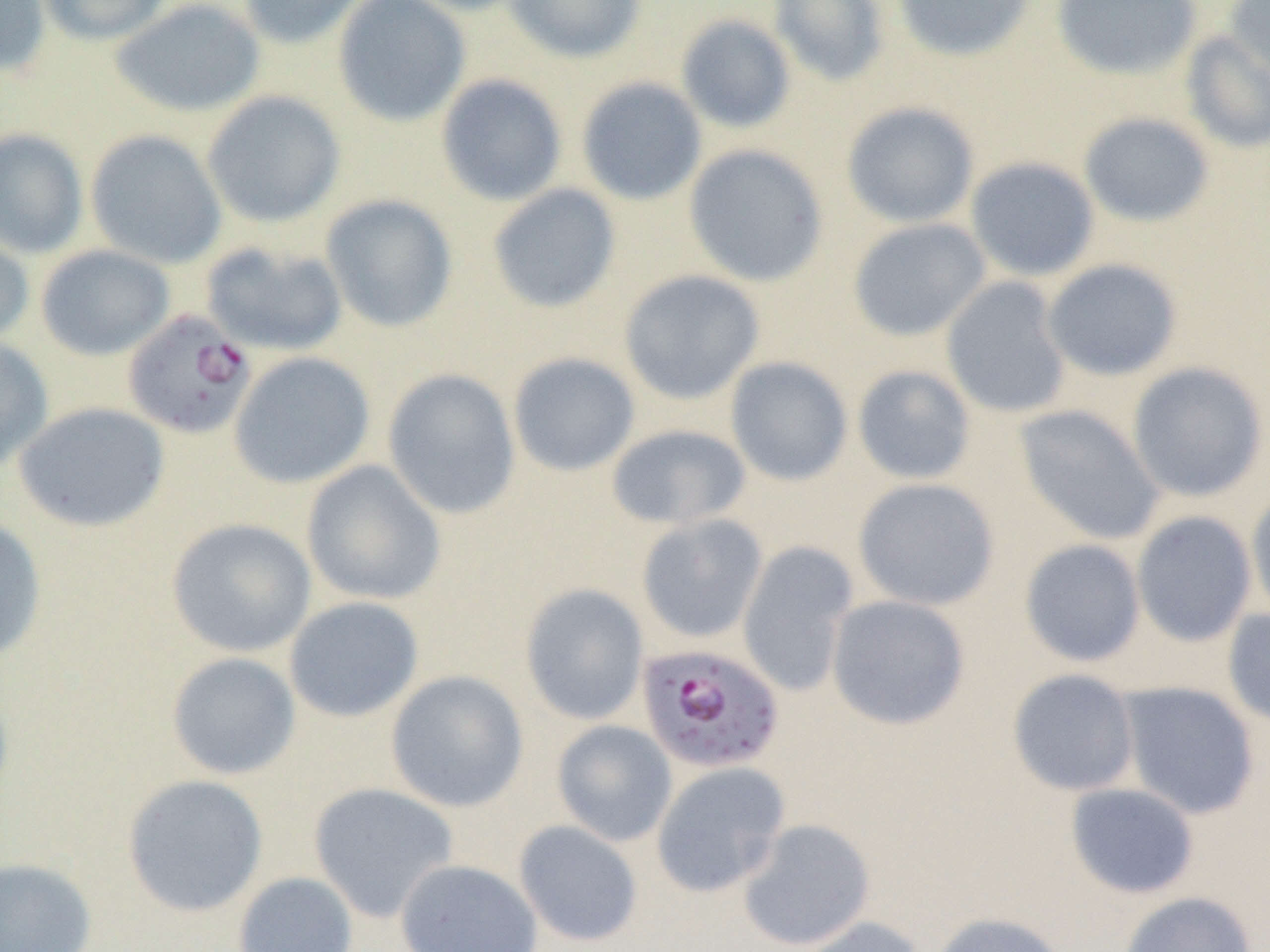
slide-level diagnosis = Plasmodium falciparum
field of view = one of a larger specimen
magnification = 1000x
modality = light microscopy
image size = 1270×952 pixels
uninfected red blood cell locations = approximate bounding boxes as (x1,y1)-(x2,y2) corner pairs in pixels: (0,0)-(51,76), (35,0)-(173,46), (110,0)-(267,118), (237,0)-(372,49), (333,0)-(471,126), (396,0)-(536,16), (504,0)-(646,64), (769,0)-(891,87), (893,0)-(1037,63), (1052,0)-(1202,81), (1225,0)-(1270,83), (675,14)-(796,134), (1180,31)-(1270,154), (436,74)-(569,207), (576,77)-(707,206), (202,90)-(346,228), (841,101)-(979,228), (1078,112)-(1215,227), (0,128)-(89,258), (85,129)-(227,269), (684,143)-(829,287), (965,156)-(1100,282), (487,183)-(622,314), (320,194)-(459,333), (848,218)-(991,342), (0,221)-(34,349), (200,240)-(348,356), (35,244)-(176,361), (1042,258)-(1183,381), (619,269)-(765,405), (941,277)-(1071,418), (0,336)-(54,472), (229,351)-(375,489), (507,352)-(641,477), (725,356)-(853,486), (1127,361)-(1268,503), (852,364)-(976,485), (383,368)-(521,520), (13,401)-(171,533), (1014,404)-(1165,546), (605,424)-(752,531), (301,460)-(447,606), (853,477)-(1000,611), (1246,486)-(1270,625), (1131,510)-(1257,647), (636,513)-(768,644), (0,515)-(48,663), (167,518)-(317,658), (1019,539)-(1146,667), (737,540)-(859,697), (519,583)-(649,725), (827,594)-(970,731), (283,596)-(424,723), (1222,608)-(1270,728), (166,651)-(301,780), (1007,668)-(1140,796), (384,669)-(529,813), (1116,681)-(1261,820), (551,719)-(678,847), (650,761)-(791,897), (121,774)-(269,918), (308,782)-(459,922), (1065,782)-(1200,899), (736,818)-(876,951), (513,819)-(643,948), (0,857)-(97,952), (394,858)-(543,952), (232,871)-(359,952), (1117,891)-(1256,952), (931,910)-(1070,952), (789,916)-(928,952)
Plasmodium falciparum-infected red blood cell locations = approximate bounding boxes as (x1,y1)-(x2,y2) corner pairs in pixels: (122,309)-(257,440), (636,642)-(786,774)
preparation = thin blood film